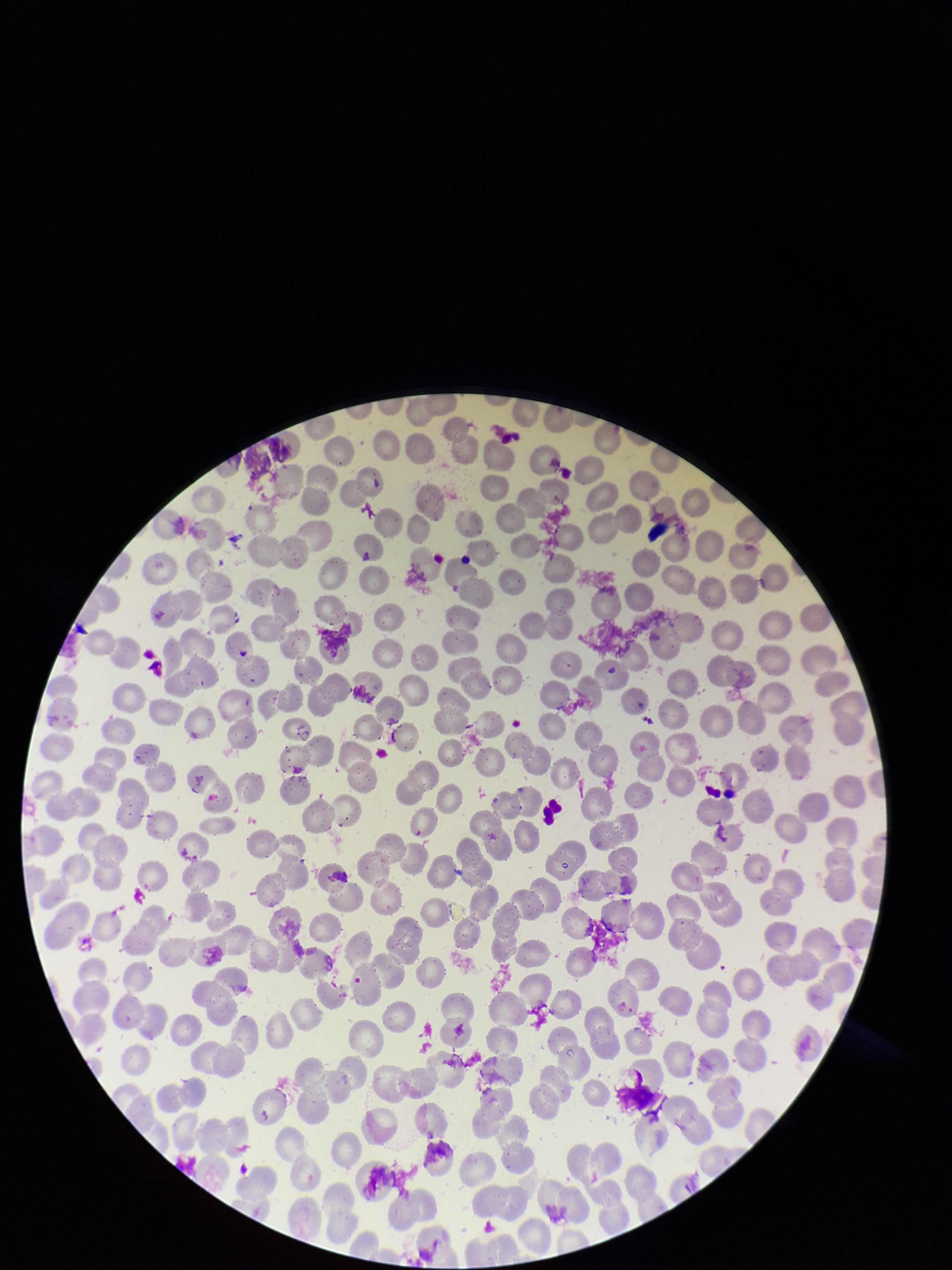

Parasitized red blood cells: none detected. Giemsa stain. Preparation: thin. Red blood cell count: 259. Parasitized red blood cell count: 0. Image is 952×1270 pixels. Patient malaria status: negative. One field from this slide. Photographed through the microscope eyepiece with a smartphone camera.